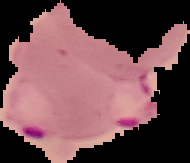

Malaria status: parasitized. From a thin blood film. Image is 190×163 pixels. Segmented cell region on a black background.